Locate every blood parasite and identify its species.
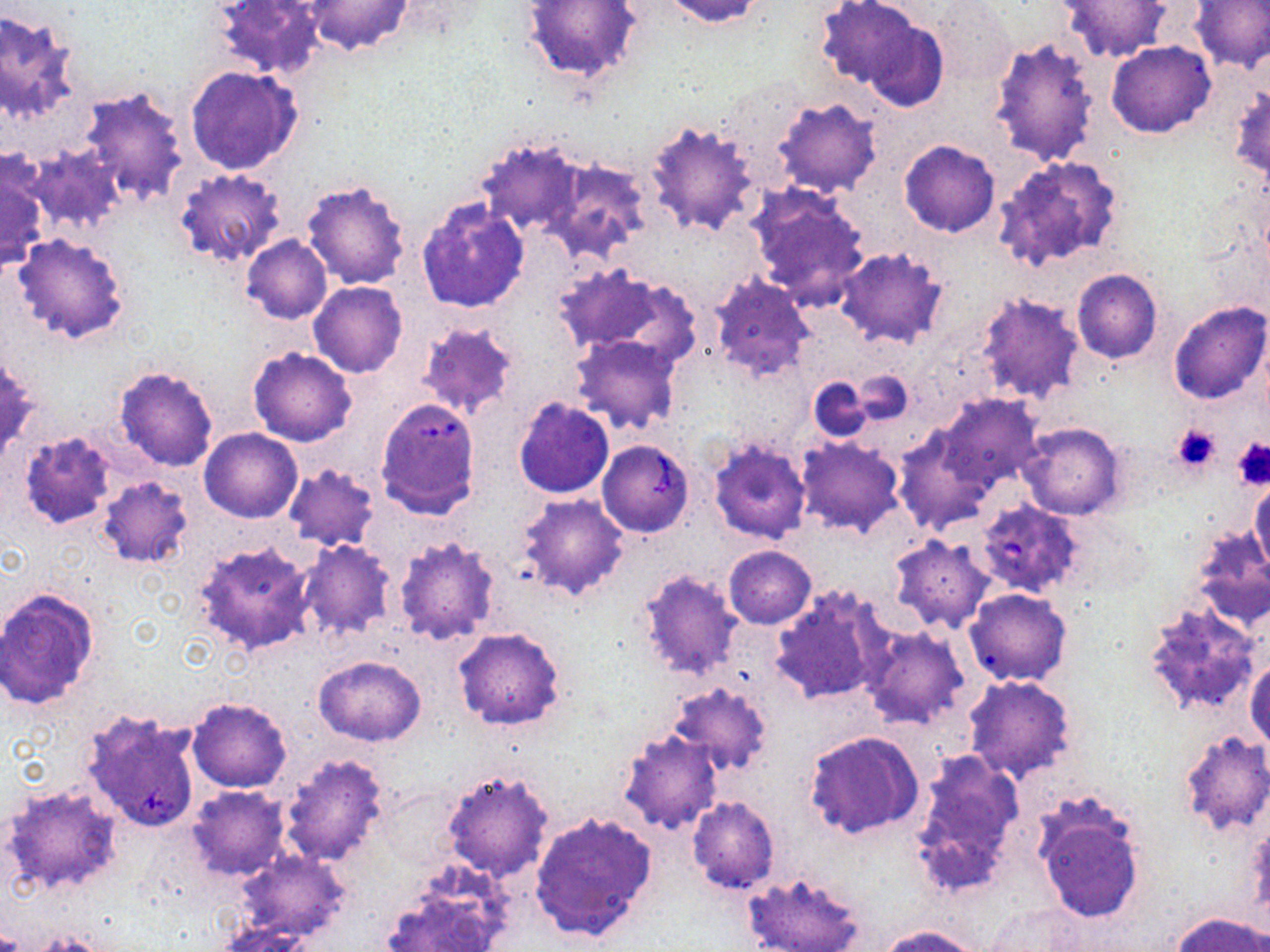

Approximate bounding boxes as named x1/y1/x2/y2 corners in pixels.
Babesia divergens-infected red blood cells: (x1=375, y1=400, x2=480, y2=521), (x1=597, y1=439, x2=693, y2=536), (x1=975, y1=500, x2=1084, y2=598).
No Plasmodium falciparum, Plasmodium ovale, Plasmodium malariae, Plasmodium vivax, or Trypanosoma brucei observed.

slide_level_diagnosis: Babesia divergens
stain: May-Grünwald-Giemsa
field_of_view: one of a larger specimen
uninfected_red_blood_cell_locations: 'approximate bounding boxes as named x1/y1/x2/y2 corners in pixels: (x1=212, y1=0, x2=326, y2=81), (x1=304, y1=0, x2=412, y2=55), (x1=523, y1=0, x2=642, y2=82), (x1=661, y1=0, x2=769, y2=28), (x1=815, y1=0, x2=924, y2=90), (x1=1191, y1=0, x2=1270, y2=73), (x1=1058, y1=1, x2=1171, y2=62), (x1=933, y1=3, x2=1014, y2=83), (x1=0, y1=9, x2=79, y2=122), (x1=863, y1=17, x2=949, y2=112), (x1=988, y1=36, x2=1100, y2=167), (x1=1108, y1=41, x2=1216, y2=138), (x1=186, y1=66, x2=303, y2=175), (x1=76, y1=84, x2=190, y2=207), (x1=771, y1=96, x2=883, y2=198), (x1=644, y1=120, x2=761, y2=237), (x1=475, y1=137, x2=586, y2=238), (x1=899, y1=140, x2=999, y2=237), (x1=24, y1=143, x2=125, y2=234), (x1=992, y1=154, x2=1124, y2=275), (x1=543, y1=156, x2=653, y2=262), (x1=0, y1=159, x2=48, y2=275), (x1=175, y1=169, x2=288, y2=266), (x1=301, y1=179, x2=410, y2=289), (x1=746, y1=183, x2=871, y2=311), (x1=416, y1=198, x2=530, y2=313), (x1=12, y1=234, x2=132, y2=345), (x1=242, y1=236, x2=332, y2=323), (x1=833, y1=245, x2=949, y2=349), (x1=553, y1=263, x2=693, y2=364), (x1=1071, y1=268, x2=1161, y2=363), (x1=708, y1=272, x2=816, y2=383), (x1=308, y1=281, x2=407, y2=377), (x1=973, y1=291, x2=1087, y2=406), (x1=1169, y1=301, x2=1269, y2=406), (x1=417, y1=321, x2=522, y2=419), (x1=571, y1=336, x2=683, y2=435), (x1=248, y1=347, x2=357, y2=447), (x1=113, y1=364, x2=220, y2=472), (x1=851, y1=372, x2=913, y2=424), (x1=809, y1=376, x2=872, y2=442), (x1=936, y1=395, x2=1042, y2=491), (x1=514, y1=397, x2=616, y2=500), (x1=1017, y1=422, x2=1126, y2=521), (x1=892, y1=427, x2=988, y2=534), (x1=199, y1=428, x2=301, y2=522), (x1=19, y1=430, x2=119, y2=528), (x1=796, y1=436, x2=904, y2=537), (x1=707, y1=439, x2=811, y2=545), (x1=282, y1=464, x2=381, y2=551), (x1=97, y1=475, x2=193, y2=569), (x1=1250, y1=478, x2=1270, y2=578), (x1=517, y1=493, x2=630, y2=600), (x1=1190, y1=528, x2=1270, y2=633), (x1=393, y1=535, x2=501, y2=645), (x1=889, y1=535, x2=995, y2=633), (x1=190, y1=538, x2=317, y2=657), (x1=297, y1=541, x2=395, y2=640), (x1=724, y1=545, x2=816, y2=628), (x1=637, y1=570, x2=741, y2=683), (x1=771, y1=585, x2=888, y2=706), (x1=0, y1=586, x2=100, y2=710), (x1=963, y1=587, x2=1073, y2=687), (x1=1144, y1=604, x2=1263, y2=717), (x1=861, y1=626, x2=970, y2=729), (x1=452, y1=627, x2=566, y2=731), (x1=314, y1=654, x2=425, y2=747), (x1=1245, y1=656, x2=1269, y2=749), (x1=962, y1=674, x2=1078, y2=782), (x1=669, y1=682, x2=772, y2=776), (x1=187, y1=697, x2=292, y2=793), (x1=618, y1=726, x2=725, y2=834), (x1=804, y1=730, x2=924, y2=841), (x1=1178, y1=731, x2=1270, y2=836), (x1=908, y1=748, x2=1025, y2=898), (x1=277, y1=752, x2=391, y2=868), (x1=440, y1=771, x2=554, y2=883), (x1=3, y1=783, x2=123, y2=897), (x1=187, y1=786, x2=292, y2=881), (x1=687, y1=796, x2=780, y2=894), (x1=1033, y1=798, x2=1146, y2=924), (x1=528, y1=810, x2=660, y2=943), (x1=232, y1=850, x2=352, y2=945), (x1=743, y1=870, x2=865, y2=952), (x1=382, y1=881, x2=507, y2=952), (x1=985, y1=901, x2=1093, y2=949), (x1=1170, y1=912, x2=1270, y2=952), (x1=215, y1=920, x2=315, y2=951), (x1=877, y1=925, x2=984, y2=952)'
modality: light microscopy
platelet_locations: 'approximate bounding boxes as named x1/y1/x2/y2 corners in pixels: (x1=1172, y1=425, x2=1222, y2=476), (x1=1230, y1=436, x2=1270, y2=489)'
preparation: thin blood smear
image_size: 1270×952 pixels
magnification: 1000x